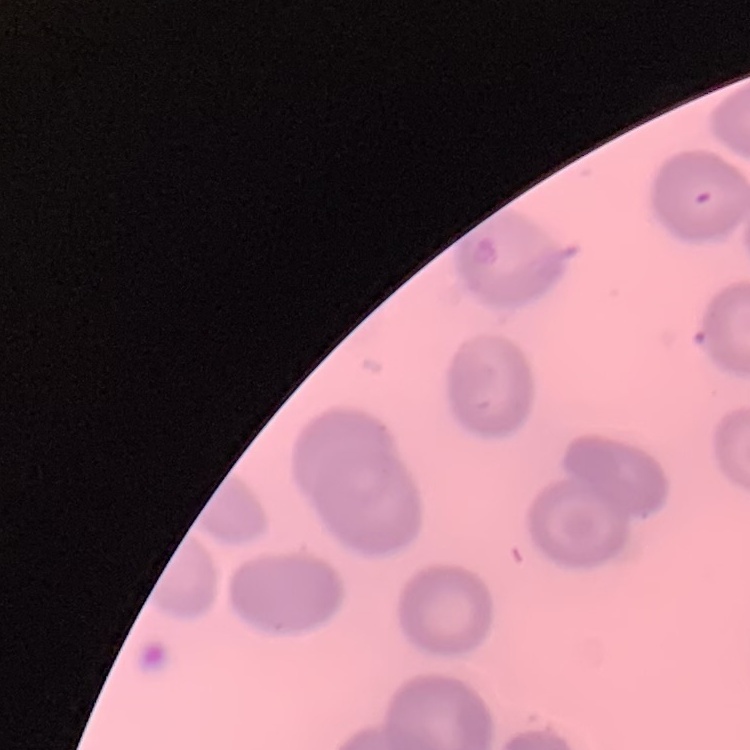
The erythrocytes exhibit no rouleaux formation. Thin blood film. One tile cut from a larger photomicrograph. Stained with either Field's or Giemsa.